Locate every Plasmodium parasite.
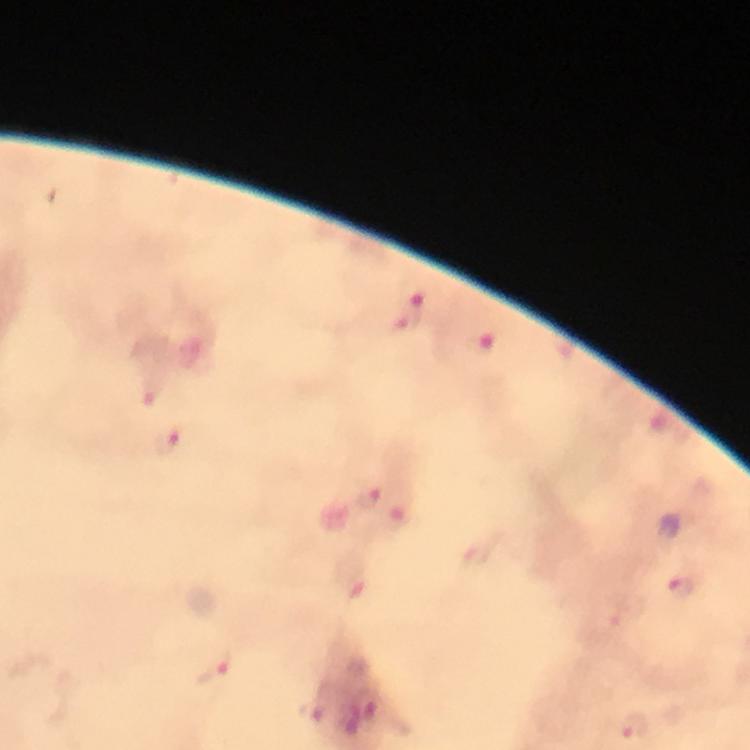
Approximate centers as {x, y} in pixels.
Plasmodium parasites: {409, 315}, {168, 442}, {369, 501}, {682, 587}, {215, 666}, {634, 726}.

cropped from = one field of view
capture = smartphone mounted on the microscope
immersion oil = applied
preparation = thick blood smear
image size = 750×750 pixels
magnification = 100x
context = from a diagnostic examination for malaria
stain = Giemsa